Describe the morphology of the red blood cells.
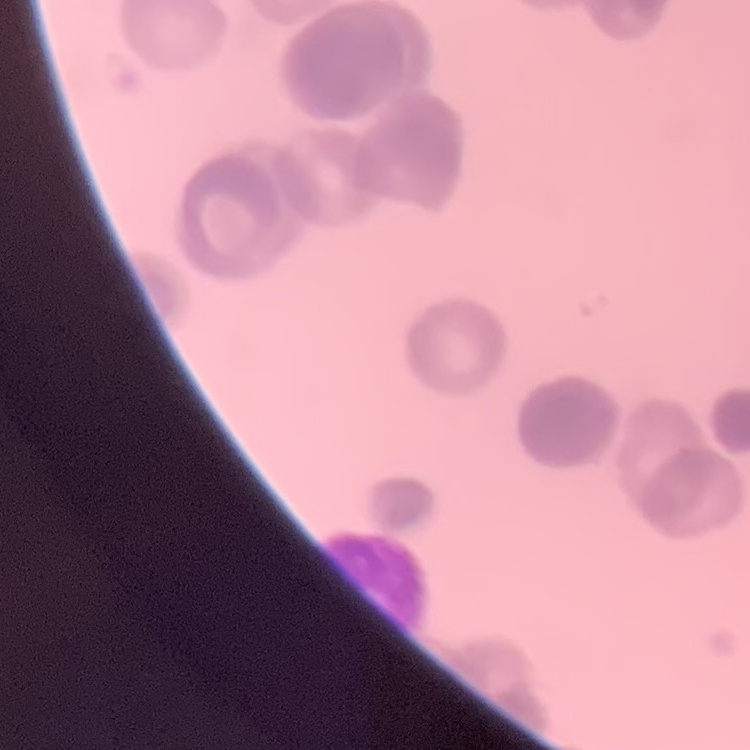

They show rouleaux formation.

Field's or Giemsa stain. One tile cut from a larger photomicrograph. Thin blood film.